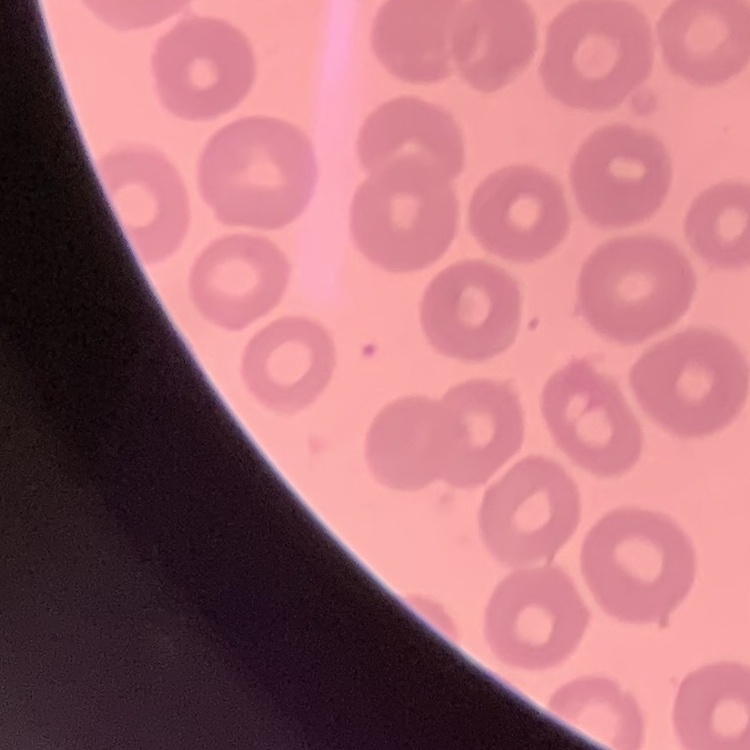

erythrocyte morphology = no rouleaux formation
image type = square crop of a larger photomicrograph
preparation = thin blood film
stain = Field's or Giemsa